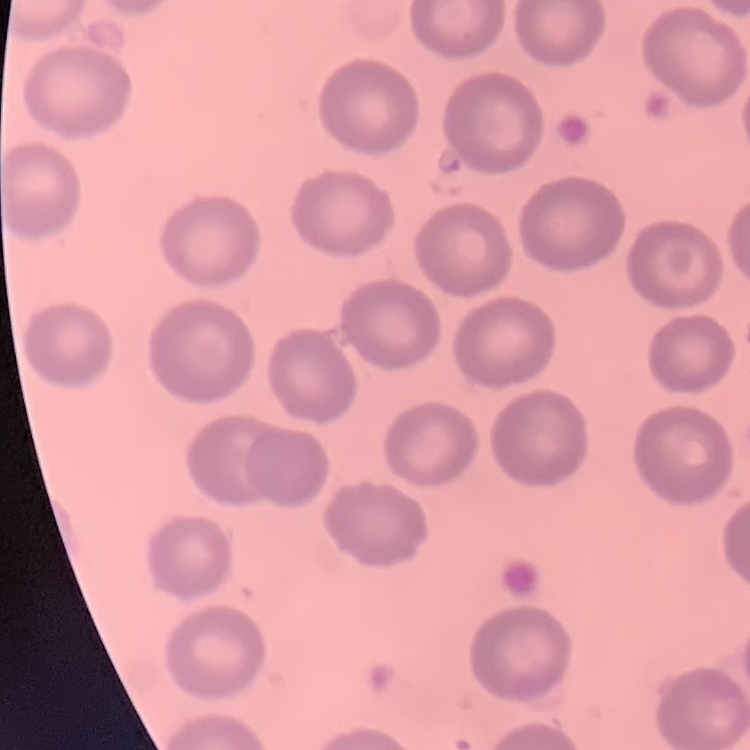

erythrocyte morphology = no rouleaux formation
image type = square crop of a larger photomicrograph
preparation = thin blood smear
stain = Field's or Giemsa